Evaluate for parasitized red blood cells.
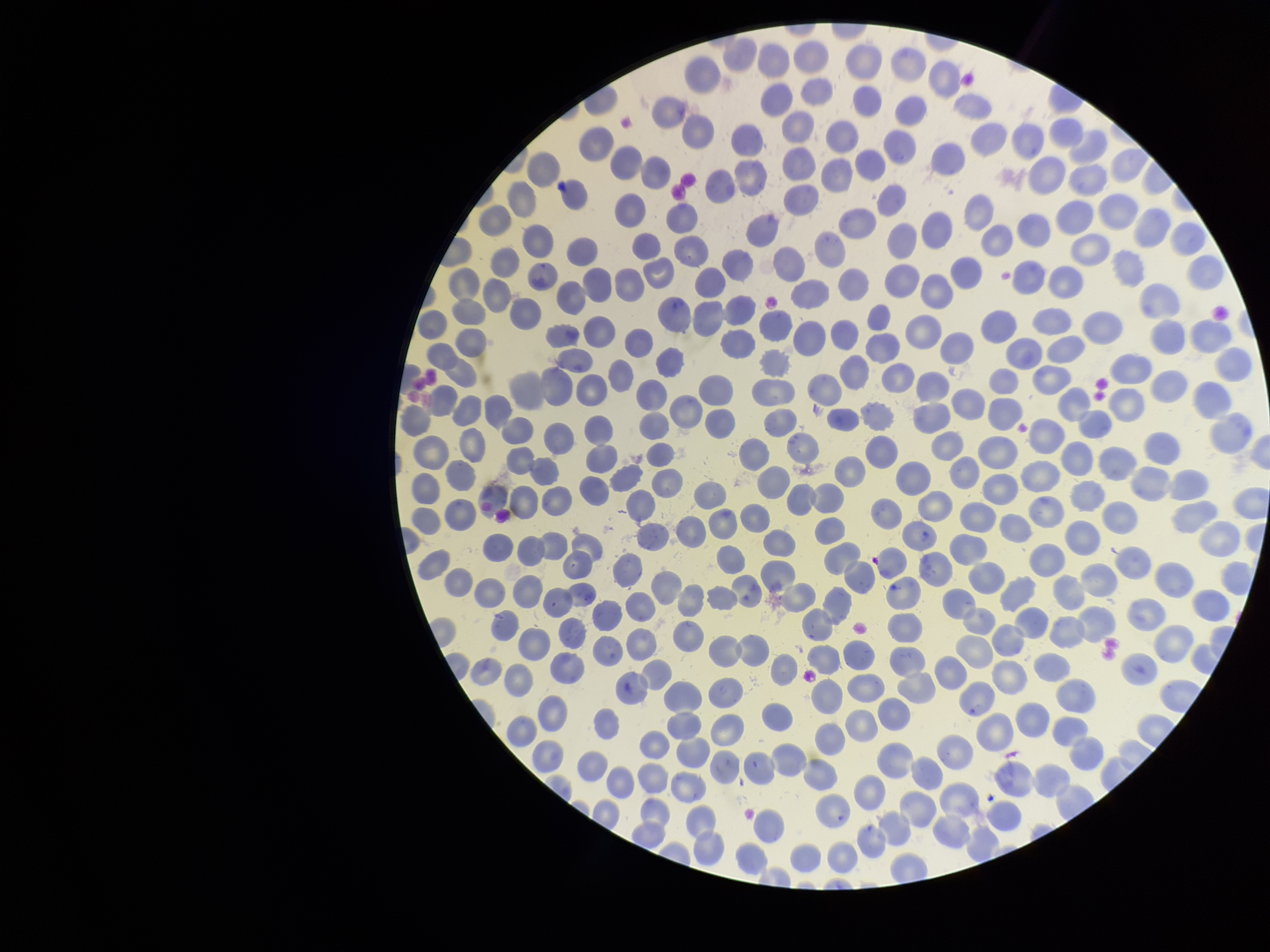

None detected.

Red blood cell count: 321. Preparation: thin smear. Giemsa stain. Patient malaria status: negative. Parasitized red blood cell count: 0. Single field of view. Image is 1270×952 pixels. Smartphone photograph taken through the eyepiece of a microscope.